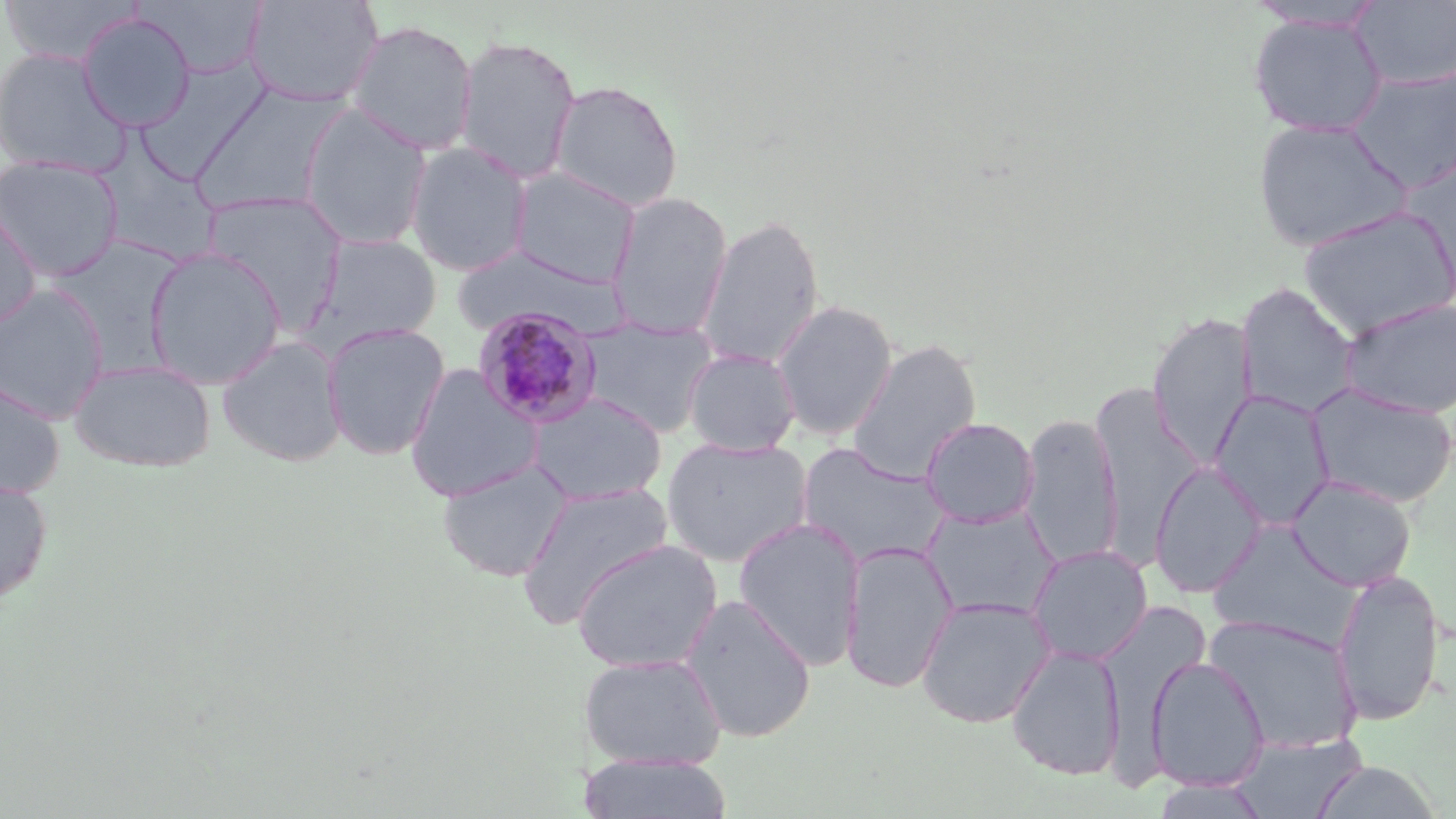

Summary:
  - Coordinate format: approximate bounding boxes as [x1, y1, x2, y2] in pixels
  - Uninfected red blood cell locations: [0, 0, 145, 67], [134, 0, 269, 80], [243, 0, 385, 107], [1350, 1, 1456, 89], [1244, 2, 1388, 32], [77, 12, 197, 132], [1247, 13, 1389, 138], [346, 19, 479, 156], [455, 35, 581, 184], [0, 48, 131, 179], [136, 57, 278, 177], [1348, 68, 1456, 192], [548, 79, 684, 213], [190, 85, 351, 217], [297, 104, 433, 251], [1251, 117, 1413, 253], [91, 135, 223, 267], [404, 141, 534, 276], [1398, 151, 1456, 302], [0, 155, 123, 282], [508, 167, 642, 287], [200, 190, 348, 330], [606, 192, 733, 340], [0, 199, 42, 331], [1298, 205, 1456, 340], [695, 214, 825, 371], [303, 233, 442, 354], [45, 236, 189, 370], [144, 246, 286, 389], [451, 246, 629, 341], [1235, 283, 1361, 418], [0, 285, 110, 423], [1339, 296, 1456, 419], [770, 300, 898, 441], [1147, 311, 1258, 468], [575, 315, 720, 438], [322, 322, 450, 460], [216, 334, 348, 468], [847, 339, 981, 485], [682, 347, 801, 456], [69, 358, 216, 472], [404, 364, 544, 503], [0, 373, 65, 498], [1306, 382, 1456, 508], [1091, 385, 1205, 558], [1209, 388, 1336, 530], [526, 392, 667, 505], [1018, 412, 1122, 568], [920, 417, 1040, 527], [661, 436, 813, 567], [796, 442, 948, 569], [436, 460, 573, 582], [1149, 461, 1268, 598], [1286, 474, 1417, 591], [0, 478, 53, 605], [515, 483, 673, 627], [921, 504, 1061, 623], [733, 517, 865, 668], [1207, 519, 1362, 649], [571, 538, 722, 673], [839, 540, 959, 694], [1027, 544, 1153, 665], [1330, 571, 1446, 725], [681, 594, 817, 743], [915, 596, 1055, 728], [1203, 614, 1363, 756], [1006, 644, 1125, 781], [579, 652, 726, 771], [1145, 655, 1270, 791], [1229, 732, 1367, 818], [580, 753, 734, 819], [1311, 761, 1442, 818], [1152, 777, 1273, 819]
  - Plasmodium malariae-infected red blood cell locations: [471, 305, 605, 430]
  - Slide-level diagnosis: Plasmodium malariae
  - Stain: May-Grünwald-Giemsa
  - Field of view: single
  - Image size: 1456×819 pixels
  - Magnification: 1000x
  - Modality: light microscopy
  - Preparation: thin blood film